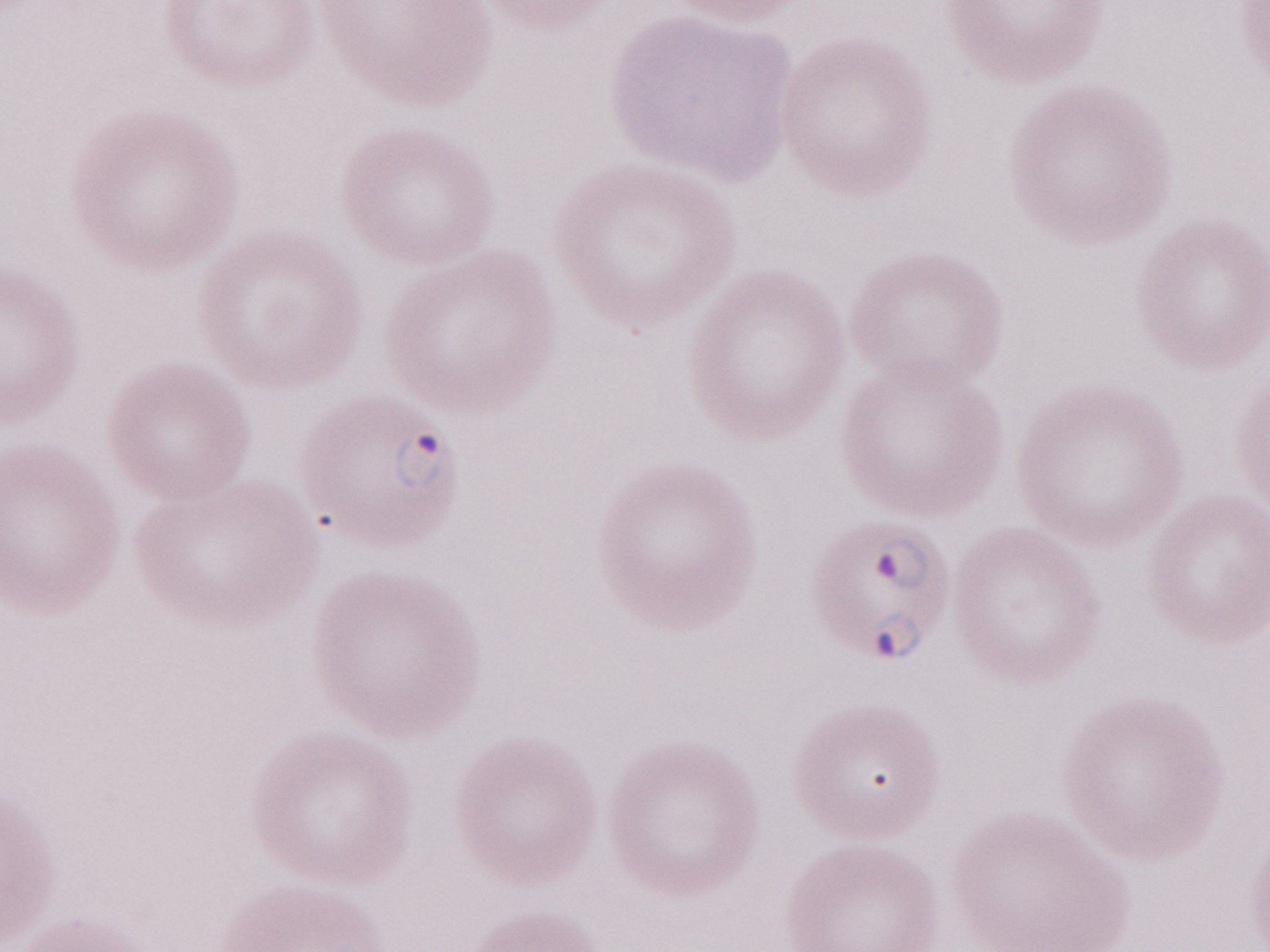 Magnification: 1,000x. May-Grünwald-Giemsa stain. Single field of view. Patient-level malaria diagnosis: positive. Olympus BX43 microscope, Olympus DP73 camera. Thin peripheral-blood smear. Image is 1270×952 pixels.